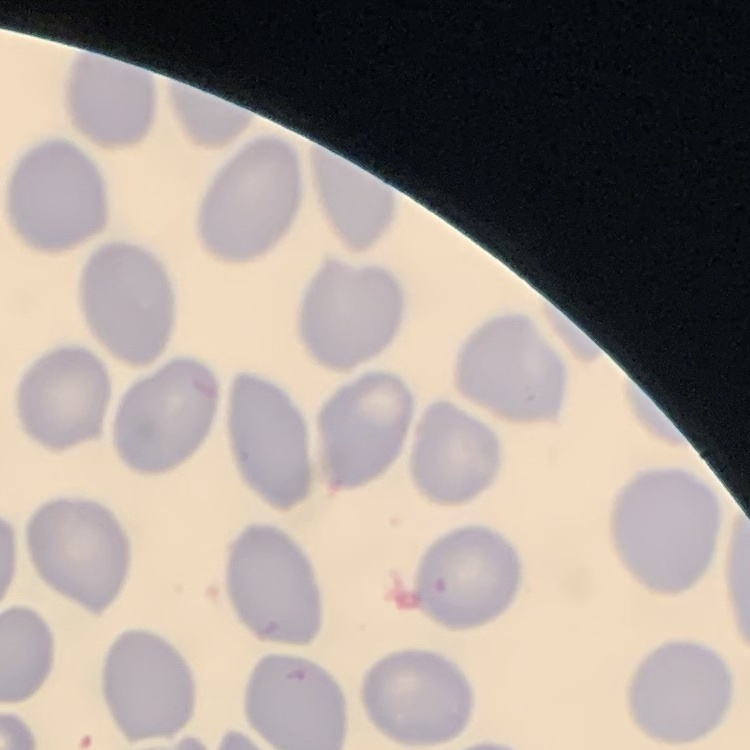
Summary:
  - Red blood cell morphology: no rouleaux formation
  - Image type: one tile cut from a larger photomicrograph
  - Stain: Field's or Giemsa
  - Preparation: thin blood smear